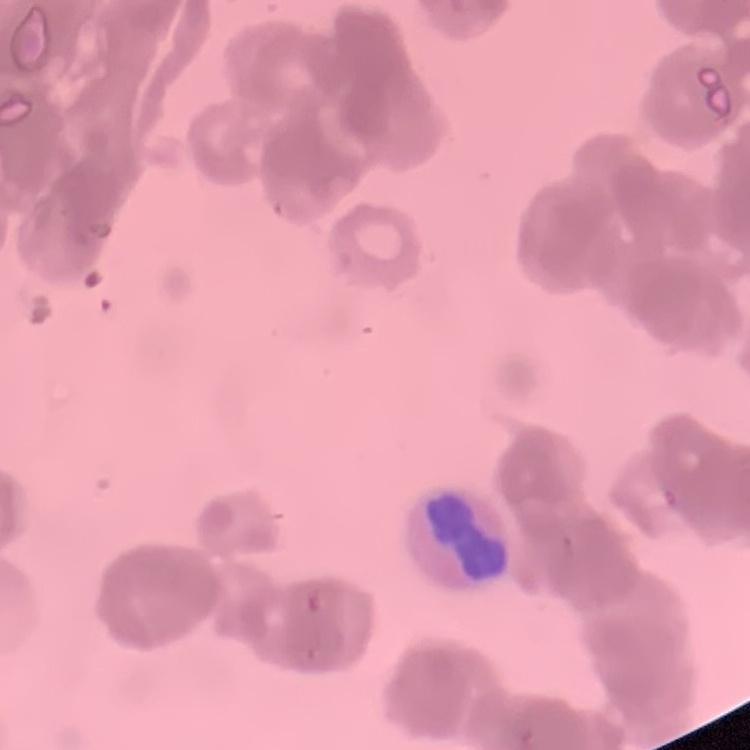

Summary:
  - Red blood cell morphology: rouleaux formation
  - Image type: square crop of a larger photomicrograph
  - Preparation: thin blood smear
  - Stain: Field's or Giemsa